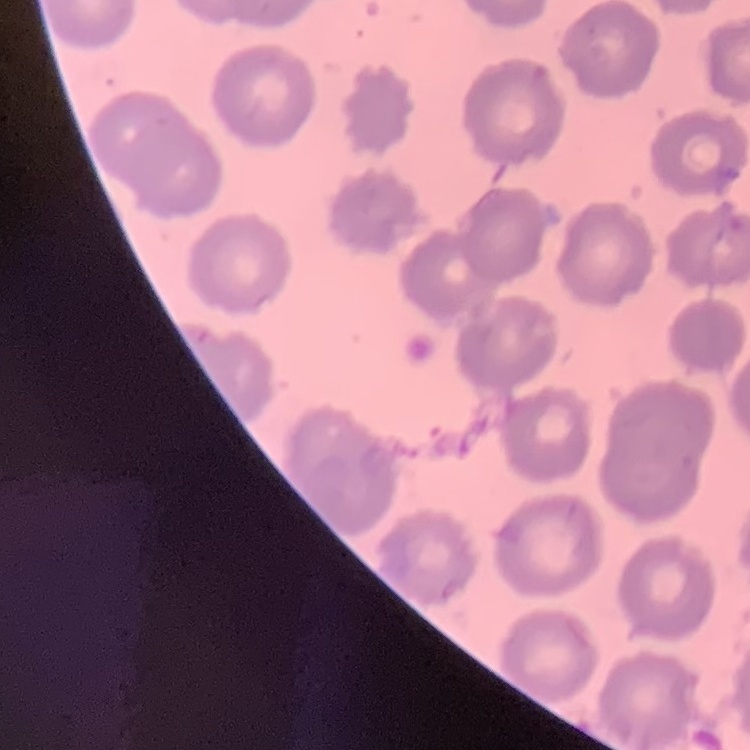

Summary:
  - Red blood cell morphology: no rouleaux formation
  - Image type: one tile cut from a larger photomicrograph
  - Stain: Field's or Giemsa
  - Preparation: thin blood film